Assess this cell for malaria.
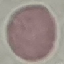
It is uninfected.

Summary:
  - Capture: smartphone through the microscope eyepiece
  - Preparation: thin smear
  - Stain: Giemsa
  - Image type: automatically extracted cell patch, resized to 64 × 64 pixels